Report the malaria status of this cell.
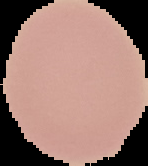

It is uninfected.

image type = segmented cell region with the area outside set to black
preparation = thin blood film
image size = 148×166 pixels